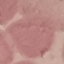

Summary:
  - Result: no malaria parasites seen
  - Stain: Giemsa
  - Capture: smartphone camera at the microscope eyepiece
  - Image type: automatically extracted cell patch, resized to 64 × 64 pixels
  - Preparation: thin blood smear